Point out each Plasmodium parasite.
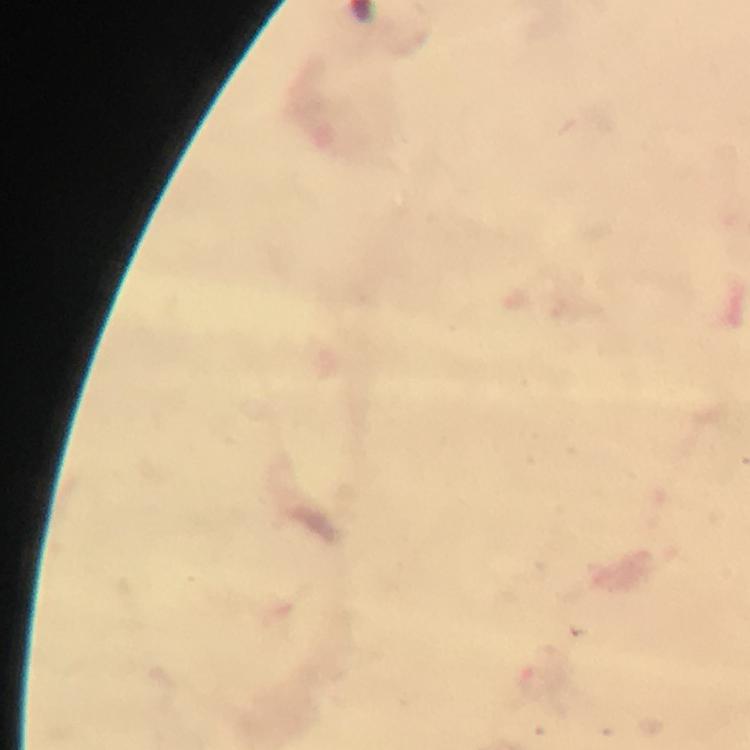

Approximate object centers, in pixels from the top-left corner.
Plasmodium parasites: (x=535, y=682).

Immersion oil applied. At 100x magnification. Image is 750×750 pixels. Thick blood film. Photographed with a smartphone mounted on the microscope. From a diagnostic examination for malaria. A crop from one field of view. Giemsa-stained preparation.